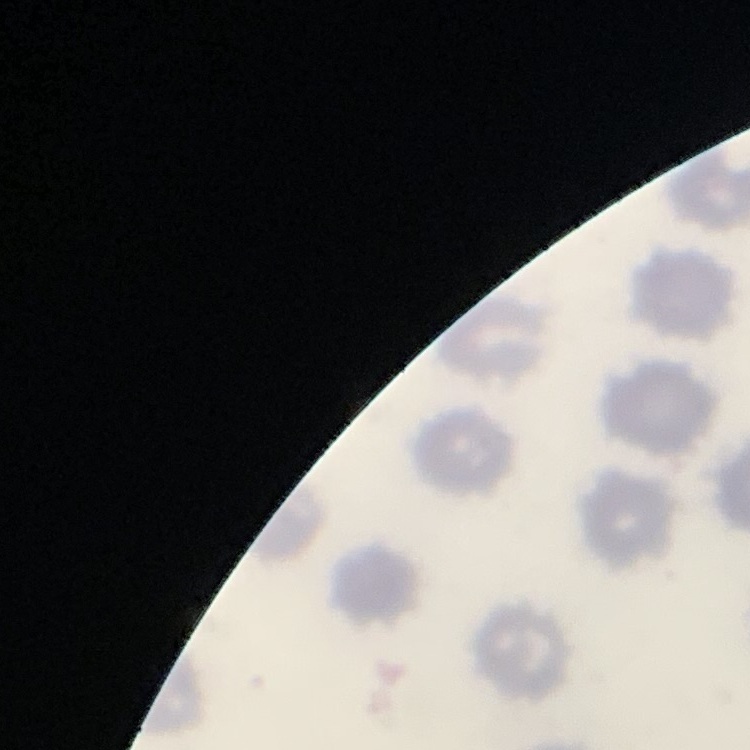
red blood cell morphology = no rouleaux formation
image type = one tile cut from a larger photomicrograph
preparation = thin blood smear
stain = Field's or Giemsa